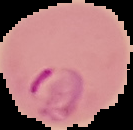

{
  "preparation": "thin blood film",
  "image_type": "cell region segmented out of the field of view; surrounding area masked to black",
  "malaria_status": "parasitized",
  "image_size": "133×130 pixels"
}